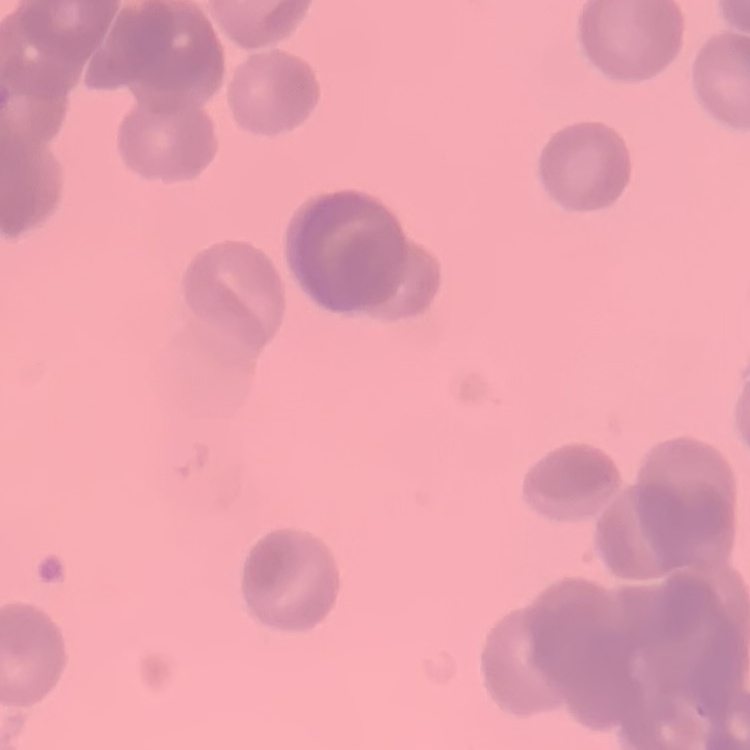

erythrocyte morphology = rouleaux formation
image type = square crop of a larger photomicrograph
preparation = thin blood smear
stain = Field's or Giemsa